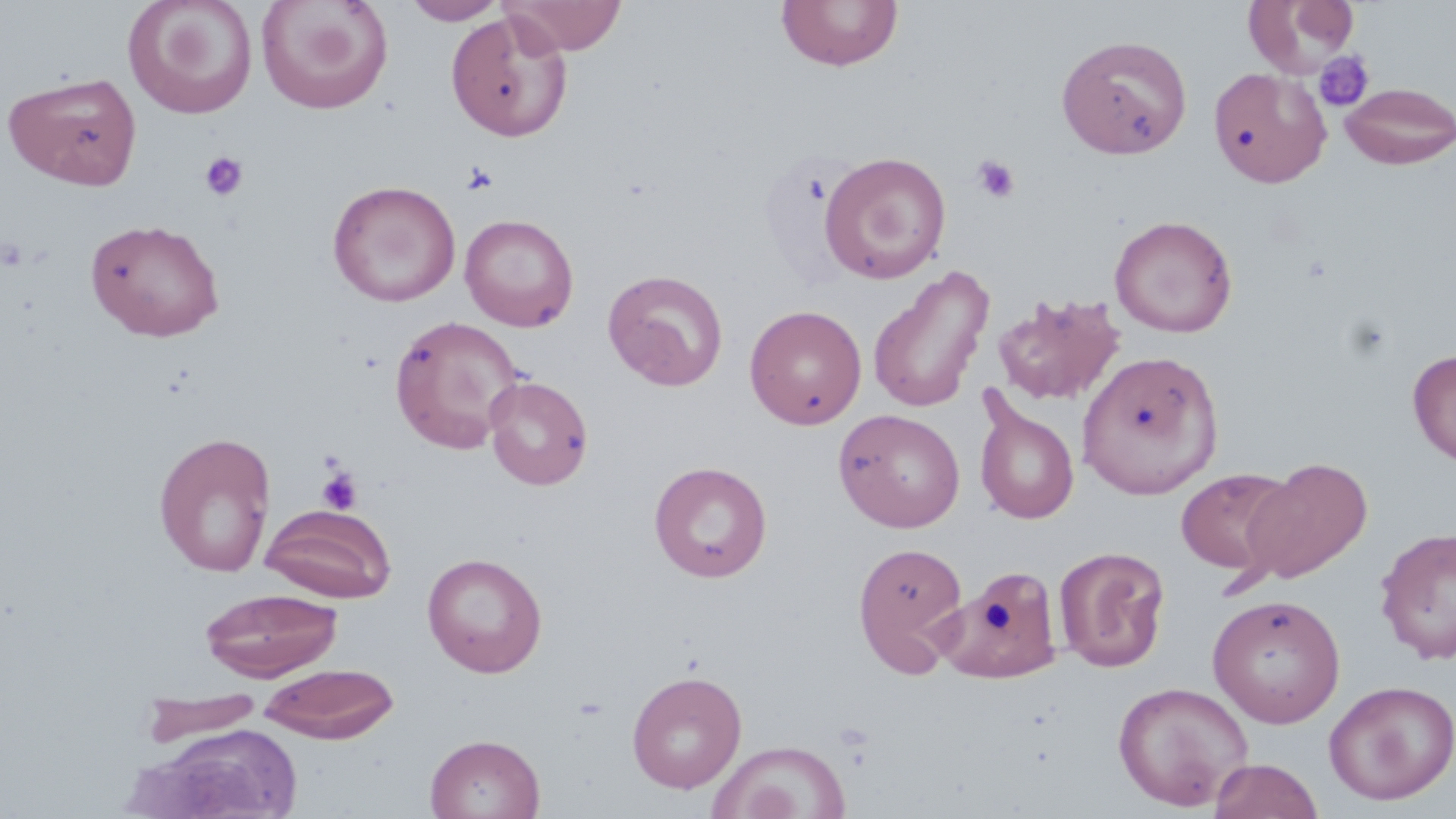

Summary:
  - Coordinate format: approximate bounding boxes as (x1, y1, x2, y2) in pixels
  - Platelet locations: (1314, 52, 1374, 111), (199, 151, 248, 201), (971, 154, 1021, 205), (461, 161, 499, 196), (317, 469, 362, 515)
  - Uninfected red blood cell locations: (122, 0, 258, 120), (256, 0, 394, 115), (403, 0, 508, 25), (503, 0, 627, 55), (776, 0, 904, 71), (1242, 0, 1362, 78), (445, 10, 573, 142), (1057, 34, 1192, 159), (1208, 66, 1331, 187), (3, 70, 143, 190), (1339, 81, 1456, 169), (819, 150, 951, 284), (328, 180, 461, 307), (459, 213, 579, 332), (1109, 214, 1238, 337), (85, 218, 225, 341), (867, 265, 995, 413), (602, 269, 728, 391), (992, 292, 1126, 407), (744, 304, 868, 430), (388, 315, 524, 454), (1077, 349, 1224, 500), (1408, 349, 1456, 467), (485, 375, 594, 490), (972, 396, 1080, 525), (833, 408, 966, 533), (153, 432, 276, 578), (1241, 457, 1374, 584), (649, 461, 772, 582), (1175, 467, 1298, 580), (262, 505, 396, 603), (1374, 526, 1456, 665), (852, 540, 969, 676), (1053, 545, 1171, 672), (422, 552, 547, 677), (940, 569, 1066, 683), (200, 587, 342, 681), (1207, 593, 1346, 728), (258, 662, 400, 744), (626, 669, 747, 794), (1323, 679, 1456, 806), (1112, 680, 1254, 811), (138, 690, 264, 749), (141, 724, 303, 818), (425, 733, 545, 818), (709, 740, 851, 819), (1209, 758, 1323, 819)
  - Slide-level diagnosis: negative for blood parasites
  - Preparation: thin blood film
  - Image size: 1456×819 pixels
  - Field of view: one of a larger specimen
  - Modality: light microscopy
  - Magnification: 1000x
  - Stain: May-Grünwald-Giemsa